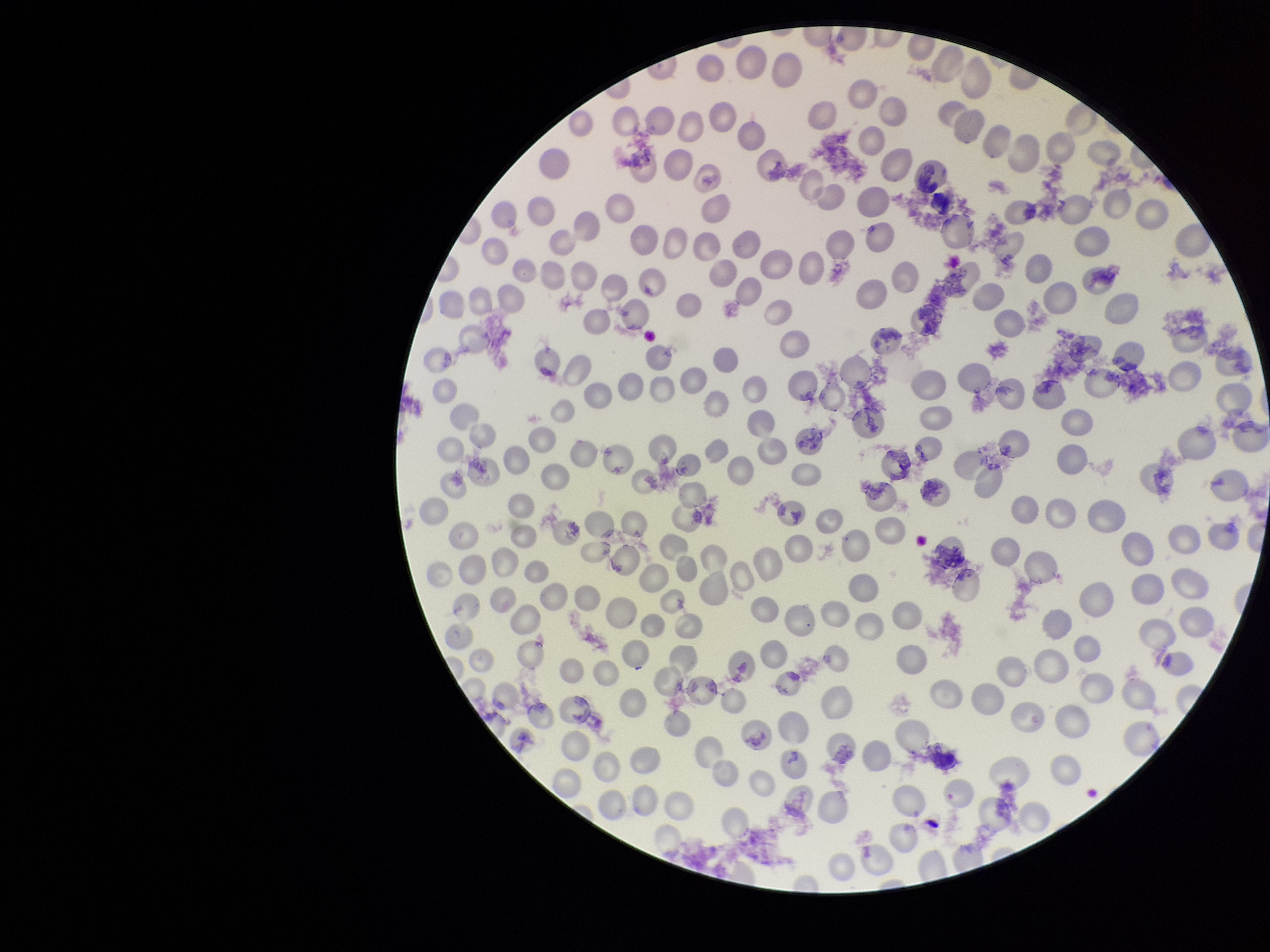
preparation = thin
image size = 1270×952 pixels
stain = Giemsa
parasitized red blood cell count = 0
capture = smartphone photograph through the microscope eyepiece
field of view = one from this slide
parasitized red blood cells = none detected
patient malaria status = positive
species reported for this patient = Plasmodium vivax
red blood cell count = 246